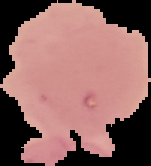
Summary:
  - Malaria status: uninfected
  - Image type: cell region segmented out of the field of view; surrounding area masked to black
  - Preparation: thin blood smear
  - Image size: 151×166 pixels